Classify this cell by malaria status.
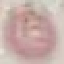
It is uninfected.

Summary:
  - Image type: automatically extracted cell patch, resized to 64 × 64 pixels
  - Capture: smartphone camera at the microscope eyepiece
  - Preparation: thin blood smear
  - Stain: Giemsa